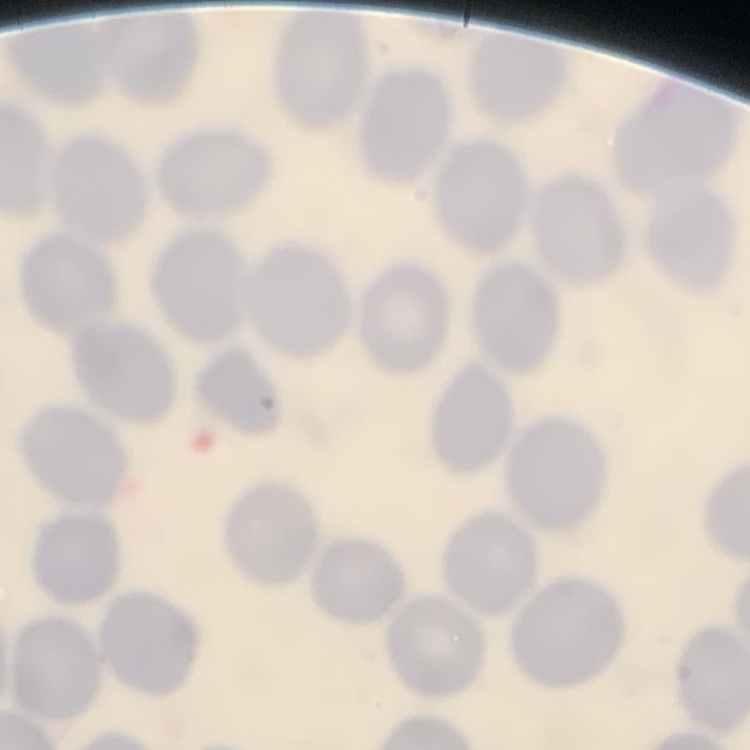

Summary:
  - Erythrocyte morphology: no rouleaux formation
  - Image type: square crop of a larger photomicrograph
  - Preparation: thin blood smear
  - Stain: Field's or Giemsa